Classify this cell by malaria status.
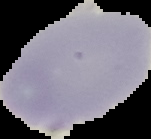
Uninfected.

Summary:
  - Image type: segmented cell region on a black background
  - Preparation: thin blood film
  - Image size: 151×139 pixels